Describe the morphology of the red blood cells.
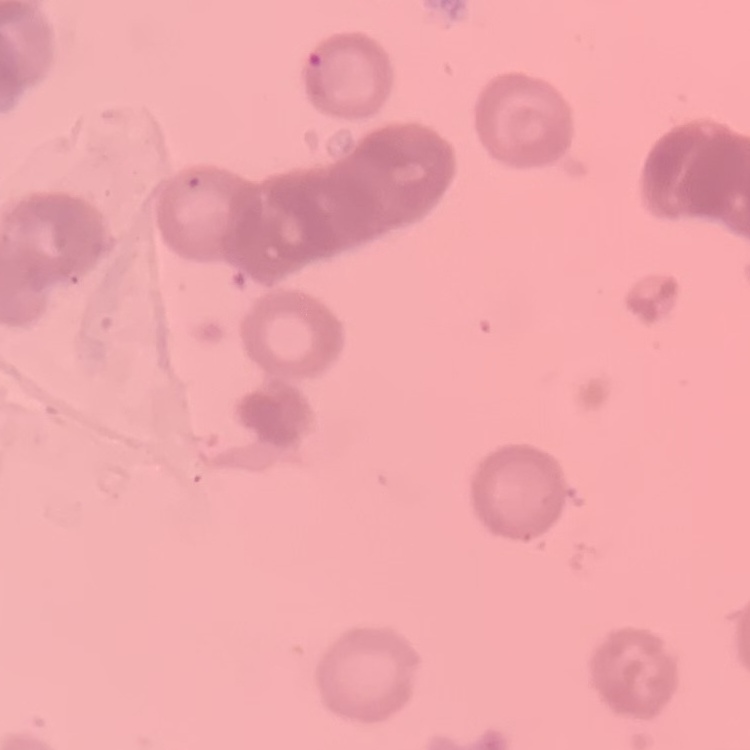

Rouleaux formation.

Square crop of a larger photomicrograph. Field's or Giemsa stain. Thin blood film.